Identify the parasite.
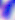

Toxoplasma gondii.

Summary:
  - Magnification: 400x
  - Modality: photomicrograph